Classify this cell by malaria status.
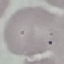
It is uninfected.

Summary:
  - Preparation: thin smear
  - Capture: smartphone camera at the microscope eyepiece
  - Image type: cell patch, automatically extracted from a larger field of view and resized to 64 × 64 pixels
  - Stain: Giemsa